State the blood parasite species.
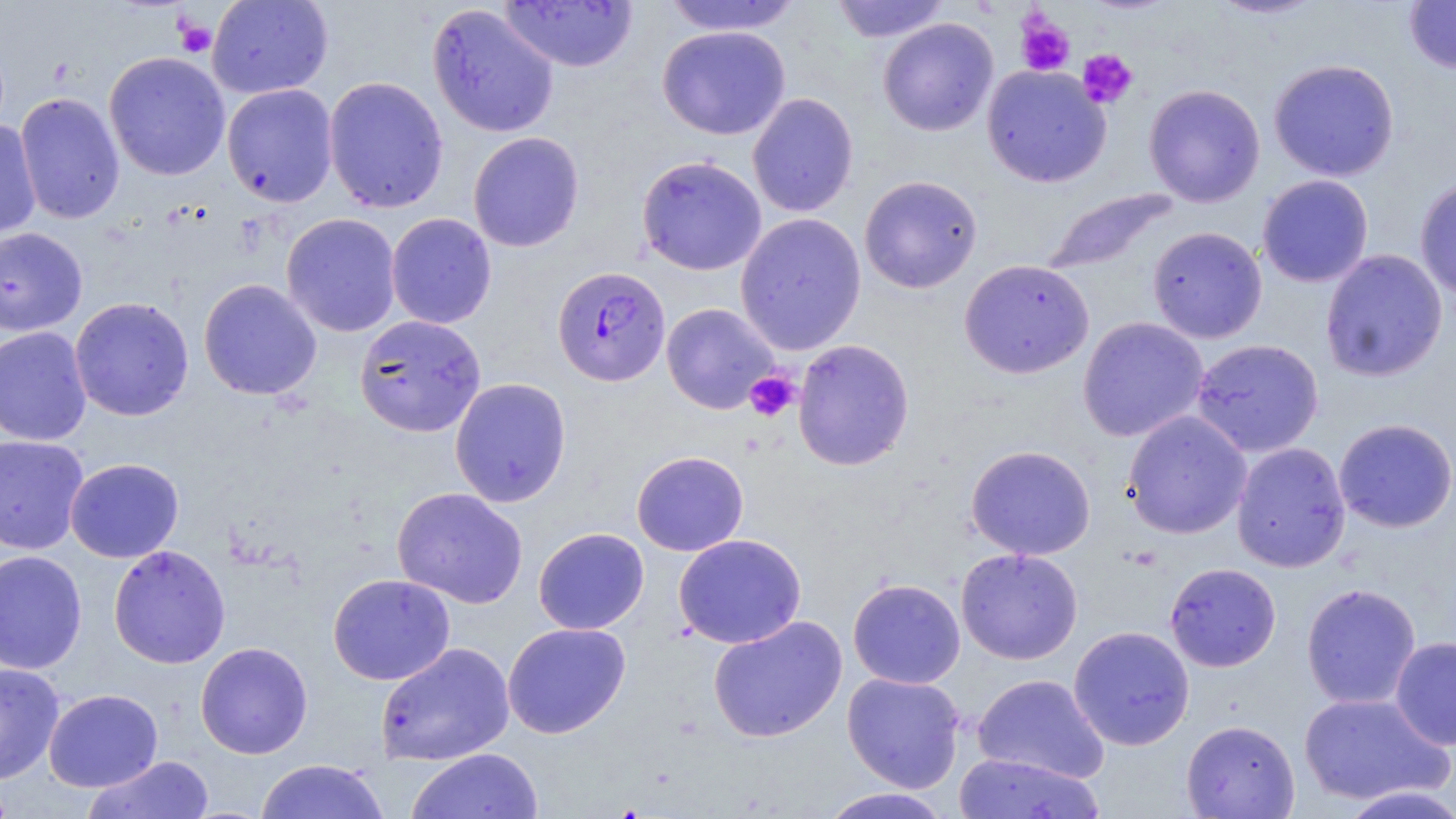
Plasmodium falciparum.

Approximate bounding boxes as [x1, y1, x2, y2] in pixels. Platelet locations: [1015, 10, 1076, 77], [173, 17, 216, 58], [1077, 49, 1138, 109], [744, 370, 800, 422]. Uninfected red blood cell locations: [207, 0, 333, 98], [661, 0, 803, 36], [829, 0, 951, 43], [1208, 0, 1326, 20], [1403, 0, 1456, 73], [499, 1, 638, 72], [426, 3, 560, 138], [878, 18, 998, 136], [657, 26, 791, 140], [104, 51, 230, 181], [1268, 58, 1400, 181], [982, 65, 1111, 187], [323, 76, 449, 213], [221, 84, 338, 207], [1143, 84, 1266, 206], [15, 92, 125, 225], [747, 92, 859, 217], [0, 119, 41, 238], [468, 131, 585, 252], [636, 155, 767, 276], [1257, 174, 1373, 288], [859, 175, 983, 294], [1414, 177, 1456, 302], [1041, 188, 1178, 275], [386, 212, 497, 329], [281, 213, 401, 337], [735, 213, 866, 355], [1147, 226, 1267, 343], [0, 227, 88, 336], [1320, 249, 1448, 382], [959, 259, 1095, 379], [198, 278, 322, 401], [69, 296, 194, 421], [661, 302, 779, 414], [354, 314, 486, 436], [1078, 317, 1209, 442], [0, 326, 92, 446], [1191, 338, 1324, 457], [792, 339, 914, 471], [449, 377, 571, 507], [1121, 410, 1251, 540], [1333, 418, 1456, 533], [0, 434, 89, 554], [1231, 442, 1351, 572], [966, 444, 1096, 560], [631, 450, 748, 556], [65, 458, 184, 562], [391, 486, 529, 608], [533, 527, 649, 634], [673, 534, 807, 648], [108, 545, 231, 669], [956, 547, 1083, 665], [0, 549, 87, 674], [1164, 562, 1281, 672], [327, 573, 456, 685], [847, 578, 965, 689], [1301, 582, 1421, 709], [708, 615, 847, 743], [502, 622, 631, 738], [1068, 626, 1195, 750], [1389, 636, 1456, 751], [195, 641, 313, 759], [375, 642, 514, 765], [0, 662, 65, 784], [842, 672, 965, 793], [972, 674, 1109, 784], [43, 688, 163, 792], [1299, 692, 1451, 806], [1181, 719, 1300, 818], [406, 748, 543, 819], [953, 752, 1106, 818], [83, 755, 215, 818], [254, 759, 389, 819], [1338, 785, 1456, 818], [817, 787, 955, 818]. Plasmodium falciparum-infected red blood cell locations: [552, 265, 671, 387]. Light microscopy. Thin blood film. Image is 1456×819 pixels. May-Grünwald-Giemsa stain. 1000x magnification. Single field of view.